Name the parasite shown.
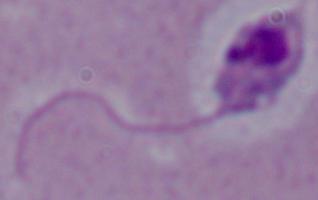
Leishmania.

Photomicrograph. 1000x magnification.